State the blood parasite species.
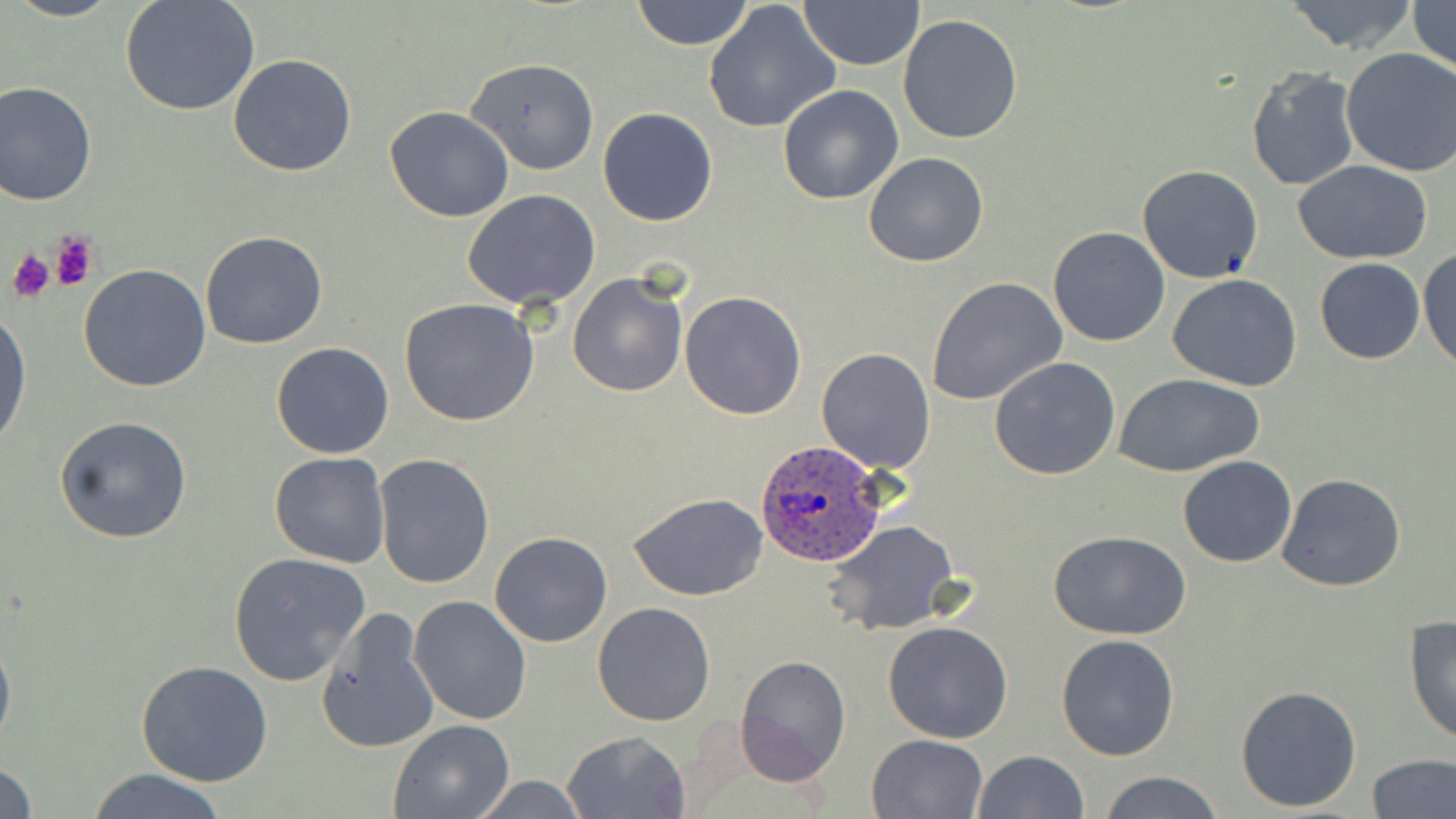
Plasmodium ovale.

Summary:
  - Coordinate format: approximate bounding boxes as named x1/y1/x2/y2 corners in pixels
  - Uninfected red blood cell locations: (x1=7, y1=0, x2=123, y2=22), (x1=120, y1=0, x2=260, y2=117), (x1=631, y1=0, x2=752, y2=49), (x1=1279, y1=0, x2=1421, y2=55), (x1=1406, y1=0, x2=1455, y2=75), (x1=702, y1=2, x2=842, y2=137), (x1=799, y1=2, x2=925, y2=71), (x1=896, y1=14, x2=1024, y2=144), (x1=1339, y1=48, x2=1456, y2=178), (x1=227, y1=53, x2=357, y2=177), (x1=466, y1=58, x2=600, y2=174), (x1=1246, y1=66, x2=1360, y2=191), (x1=0, y1=80, x2=98, y2=206), (x1=777, y1=84, x2=905, y2=204), (x1=385, y1=106, x2=513, y2=222), (x1=597, y1=107, x2=719, y2=226), (x1=864, y1=151, x2=988, y2=268), (x1=1293, y1=161, x2=1433, y2=264), (x1=1136, y1=164, x2=1264, y2=284), (x1=462, y1=191, x2=603, y2=310), (x1=1048, y1=226, x2=1171, y2=347), (x1=200, y1=231, x2=327, y2=349), (x1=1418, y1=247, x2=1456, y2=371), (x1=1314, y1=258, x2=1425, y2=364), (x1=78, y1=264, x2=211, y2=393), (x1=567, y1=274, x2=688, y2=396), (x1=1167, y1=274, x2=1301, y2=391), (x1=927, y1=276, x2=1067, y2=406), (x1=679, y1=290, x2=807, y2=419), (x1=400, y1=299, x2=539, y2=428), (x1=0, y1=310, x2=31, y2=450), (x1=271, y1=342, x2=395, y2=459), (x1=817, y1=346, x2=936, y2=474), (x1=988, y1=356, x2=1121, y2=480), (x1=1114, y1=373, x2=1265, y2=476), (x1=54, y1=415, x2=193, y2=543), (x1=270, y1=453, x2=391, y2=569), (x1=372, y1=454, x2=495, y2=590), (x1=1177, y1=457, x2=1297, y2=568), (x1=1276, y1=472, x2=1406, y2=591), (x1=629, y1=493, x2=768, y2=602), (x1=828, y1=522, x2=959, y2=634), (x1=490, y1=531, x2=613, y2=647), (x1=1049, y1=531, x2=1190, y2=640), (x1=227, y1=551, x2=370, y2=685), (x1=407, y1=595, x2=531, y2=726), (x1=593, y1=601, x2=716, y2=725), (x1=315, y1=608, x2=440, y2=755), (x1=1405, y1=615, x2=1456, y2=746), (x1=883, y1=620, x2=1013, y2=743), (x1=0, y1=624, x2=15, y2=758), (x1=1056, y1=632, x2=1180, y2=760), (x1=735, y1=656, x2=852, y2=785), (x1=136, y1=661, x2=272, y2=787), (x1=1235, y1=684, x2=1362, y2=813), (x1=389, y1=719, x2=513, y2=818), (x1=562, y1=730, x2=692, y2=819), (x1=868, y1=733, x2=988, y2=818), (x1=974, y1=749, x2=1087, y2=819), (x1=1367, y1=753, x2=1455, y2=819), (x1=0, y1=760, x2=38, y2=819), (x1=86, y1=767, x2=229, y2=819), (x1=1099, y1=772, x2=1224, y2=819), (x1=467, y1=774, x2=593, y2=817)
  - Plasmodium ovale-infected red blood cell locations: (x1=754, y1=439, x2=884, y2=567)
  - Platelet locations: (x1=49, y1=229, x2=100, y2=291), (x1=5, y1=249, x2=54, y2=303)
  - Stain: May-Grünwald-Giemsa
  - Preparation: thin blood film
  - Modality: optical microscopy
  - Magnification: 1000x
  - Field of view: one of a larger specimen
  - Image size: 1456×819 pixels